Classify this cell by malaria status.
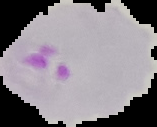
It is parasitized.

Summary:
  - Image type: segmented cell region on a black background
  - Preparation: thin blood film
  - Image size: 157×127 pixels